Report the malaria status of this cell.
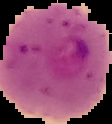
It is parasitized.

Summary:
  - Image size: 112×124 pixels
  - Image type: cell region segmented out of the field of view; surrounding area masked to black
  - Preparation: thin blood film